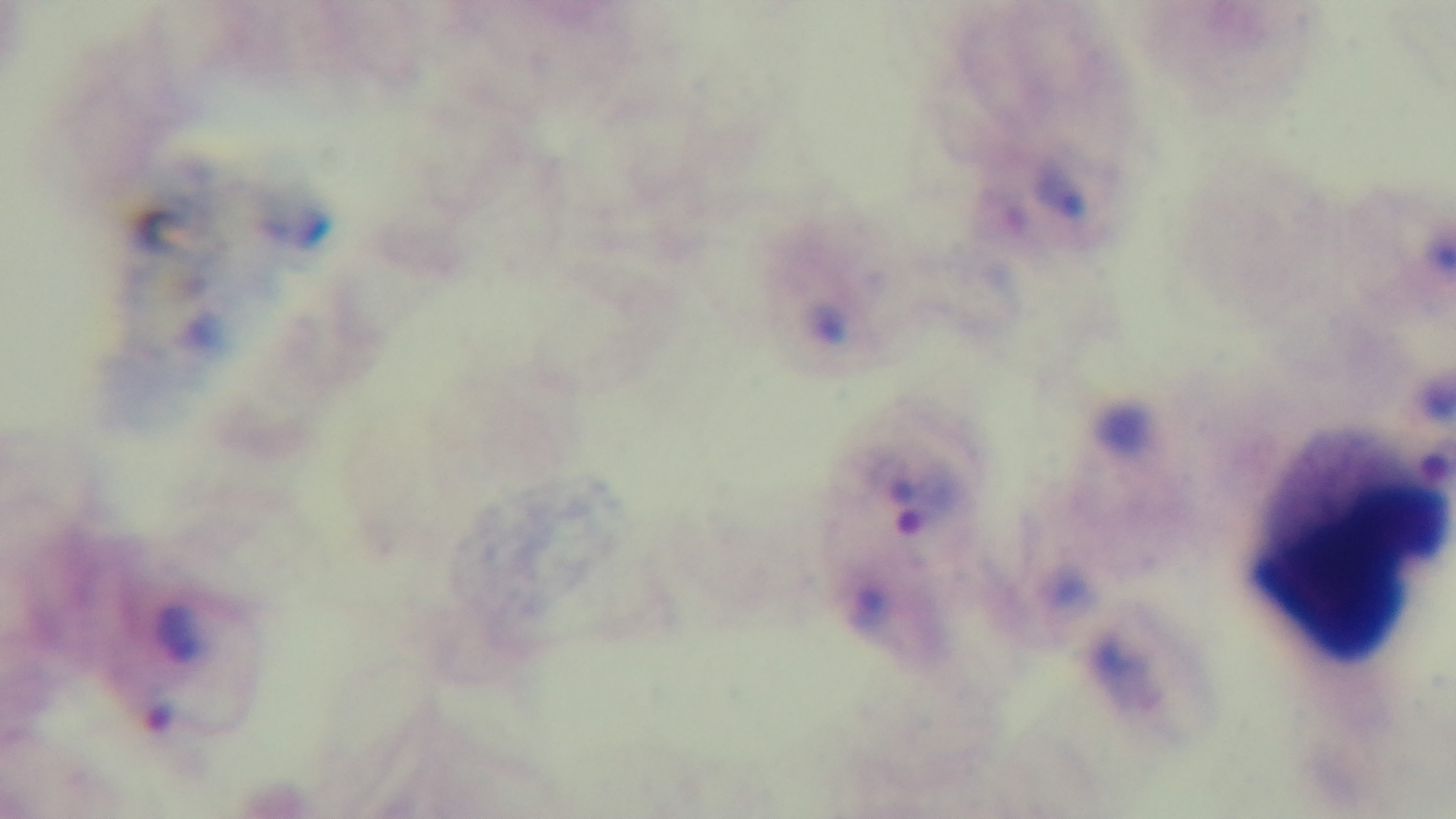
Summary:
  - Objective: 100x oil immersion
  - Modality: light microscopy
  - Stain: Giemsa
  - Capture: mounted 4K digital camera
  - Preparation: thick
  - Field of view: single
  - Malaria status: positive